Locate every uninfected red blood cell.
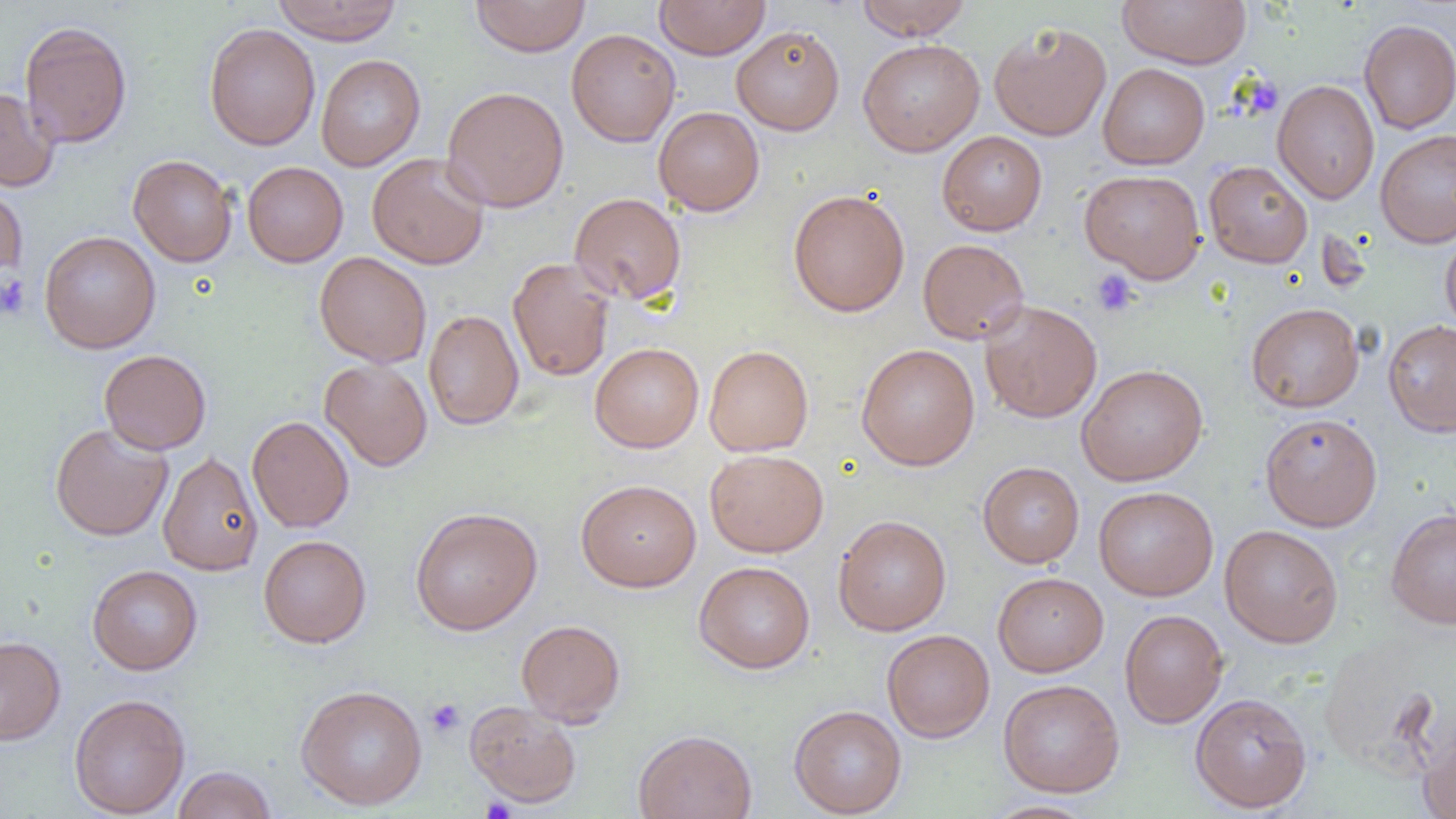
Approximate bounding boxes as [x1, y1, x2, y2] in pixels.
Uninfected red blood cells: [271, 0, 403, 44], [471, 0, 590, 57], [654, 0, 771, 59], [856, 0, 972, 40], [1117, 0, 1252, 68], [1359, 19, 1456, 134], [19, 20, 132, 148], [989, 21, 1112, 141], [204, 23, 321, 150], [732, 25, 845, 135], [566, 28, 680, 147], [857, 38, 984, 156], [316, 54, 426, 171], [1098, 62, 1210, 169], [1272, 79, 1380, 204], [441, 86, 569, 212], [0, 87, 59, 192], [653, 106, 765, 216], [1375, 129, 1456, 247], [937, 131, 1047, 235], [367, 152, 490, 270], [127, 154, 238, 266], [1203, 160, 1313, 268], [242, 161, 348, 267], [1079, 169, 1206, 283], [0, 180, 28, 279], [788, 188, 910, 317], [569, 192, 687, 306], [1440, 230, 1456, 337], [39, 231, 161, 353], [917, 238, 1029, 345], [314, 251, 432, 368], [508, 257, 614, 382], [979, 299, 1102, 423], [1246, 302, 1364, 412], [423, 310, 524, 430], [1382, 319, 1456, 437], [590, 342, 704, 452], [856, 343, 980, 471], [704, 345, 813, 456], [99, 349, 211, 454], [319, 359, 433, 472], [1076, 363, 1208, 486], [1260, 412, 1383, 531], [247, 416, 354, 533], [50, 423, 173, 541], [705, 449, 828, 557], [158, 450, 263, 576], [978, 461, 1084, 567], [576, 478, 701, 592], [1093, 486, 1219, 601], [410, 507, 542, 635], [1386, 507, 1456, 629], [833, 514, 952, 636], [1219, 524, 1344, 648], [258, 535, 371, 648], [694, 561, 815, 673], [87, 565, 203, 675], [992, 572, 1108, 676], [1119, 609, 1229, 728], [516, 619, 626, 727], [881, 629, 995, 742], [1317, 634, 1451, 780], [0, 636, 66, 745], [998, 678, 1125, 797], [295, 684, 428, 811], [1189, 692, 1313, 812], [69, 693, 190, 818], [465, 701, 582, 808], [788, 705, 907, 817], [1418, 724, 1456, 819], [633, 728, 758, 819], [172, 765, 277, 819], [983, 800, 1098, 819].

Summary:
  - Platelet locations: [1253, 80, 1278, 111], [1091, 269, 1139, 317], [0, 275, 32, 321], [425, 698, 466, 738], [481, 797, 516, 819]
  - Slide-level diagnosis: no evidence of blood parasites
  - Field of view: one of a larger specimen
  - Image size: 1456×819 pixels
  - Preparation: thin blood film
  - Modality: light microscopy
  - Magnification: 1000x